Classify this cell by malaria status.
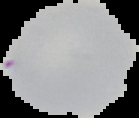

It is uninfected.

Segmented cell region on a black background. From a thin blood smear. Image is 139×118 pixels.